Classify this cell by malaria status.
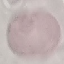
It is uninfected.

Thin blood smear. Photographed with a smartphone camera at the microscope eyepiece. Automatically extracted cell patch, resized to 64 × 64 pixels. Giemsa-stained preparation.